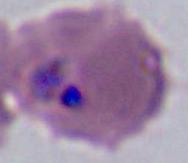

Photomicrograph. A Plasmodium parasite is shown. Captured at either 400x or 1000x magnification.